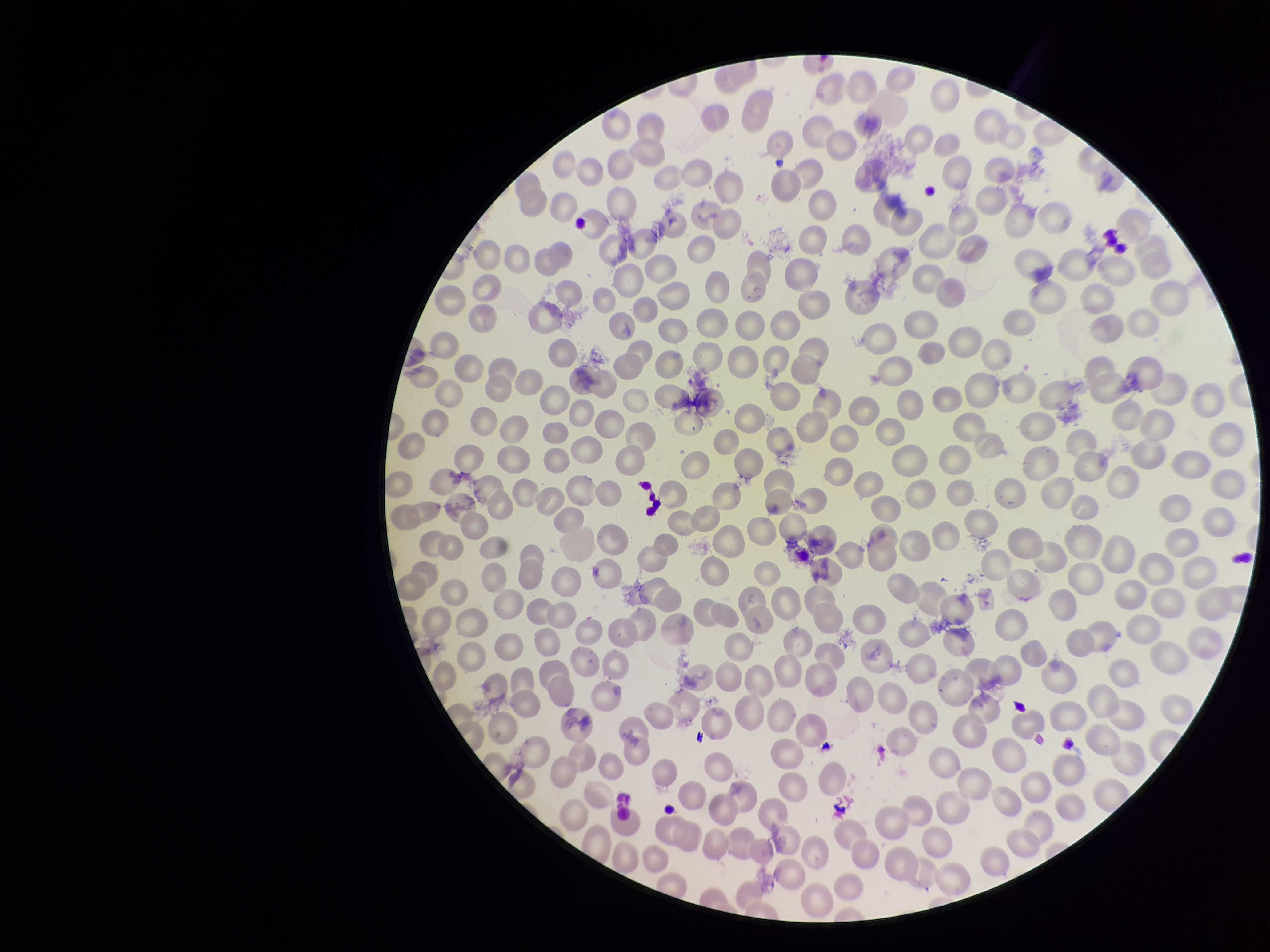
species reported for this patient = Plasmodium falciparum
parasitized red blood cell count = 0
image size = 1270×952 pixels
stain = Giemsa
red blood cell count = 315
parasitized red blood cells = none seen
capture = smartphone photograph through the microscope eyepiece
field of view = single
patient malaria status = infected
preparation = thin